Classify this cell by malaria status.
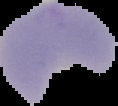

It is parasitized.

Summary:
  - Image size: 118×106 pixels
  - Image type: cell region segmented out of the field of view; surrounding area masked to black
  - Preparation: thin blood film